Comment on the morphology of the erythrocytes.
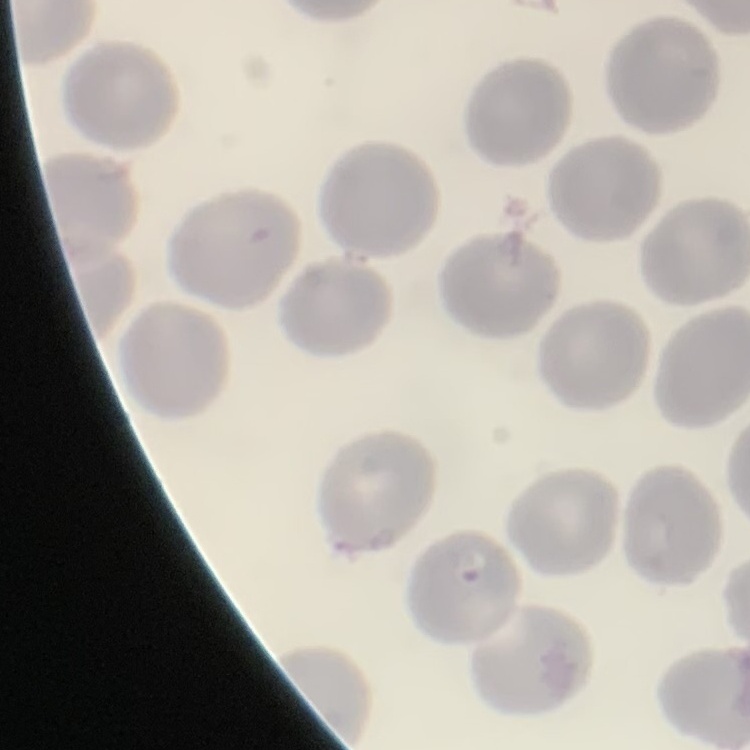
They show no rouleaux formation.

stain = Field's or Giemsa
preparation = thin blood smear
image type = one tile cut from a larger photomicrograph